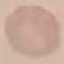
malaria_status: uninfected
stain: Giemsa
image_type: cell patch, automatically extracted from a larger field of view and resized to 64 × 64 pixels
preparation: thin smear
capture: smartphone through the microscope eyepiece